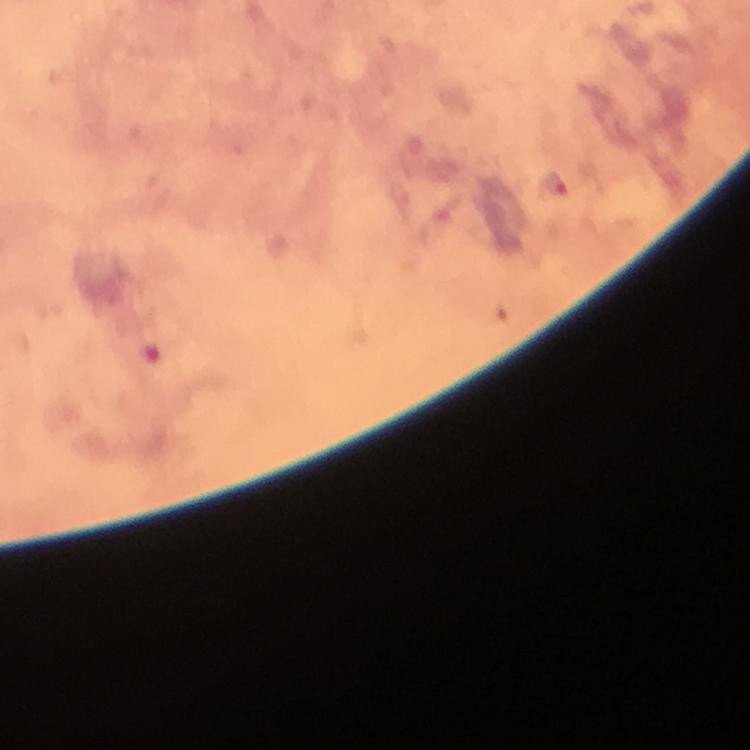
Approximate object centers, in pixels from the top-left corner. Malaria parasite locations: (x=557, y=186). From a diagnostic examination for malaria. At 100x magnification. Immersion oil applied. Giemsa stain. Image is 750×750 pixels. Cropped region of a single field of view. Thick blood smear. Smartphone photograph taken through a microscope.